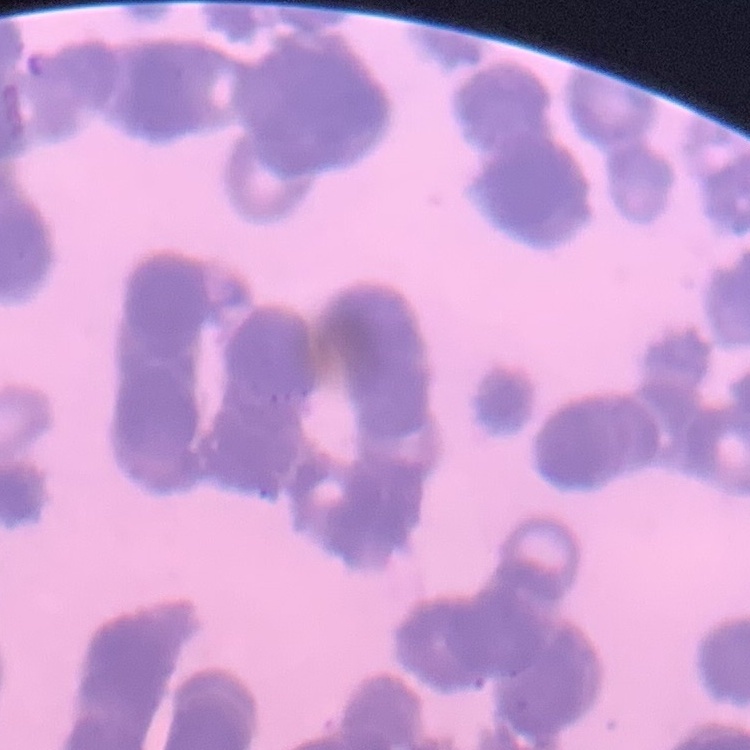

Summary:
  - Erythrocyte morphology: rouleaux formation
  - Image type: square crop of a larger photomicrograph
  - Preparation: thin blood film
  - Stain: Field's or Giemsa